Mark where platelets are.
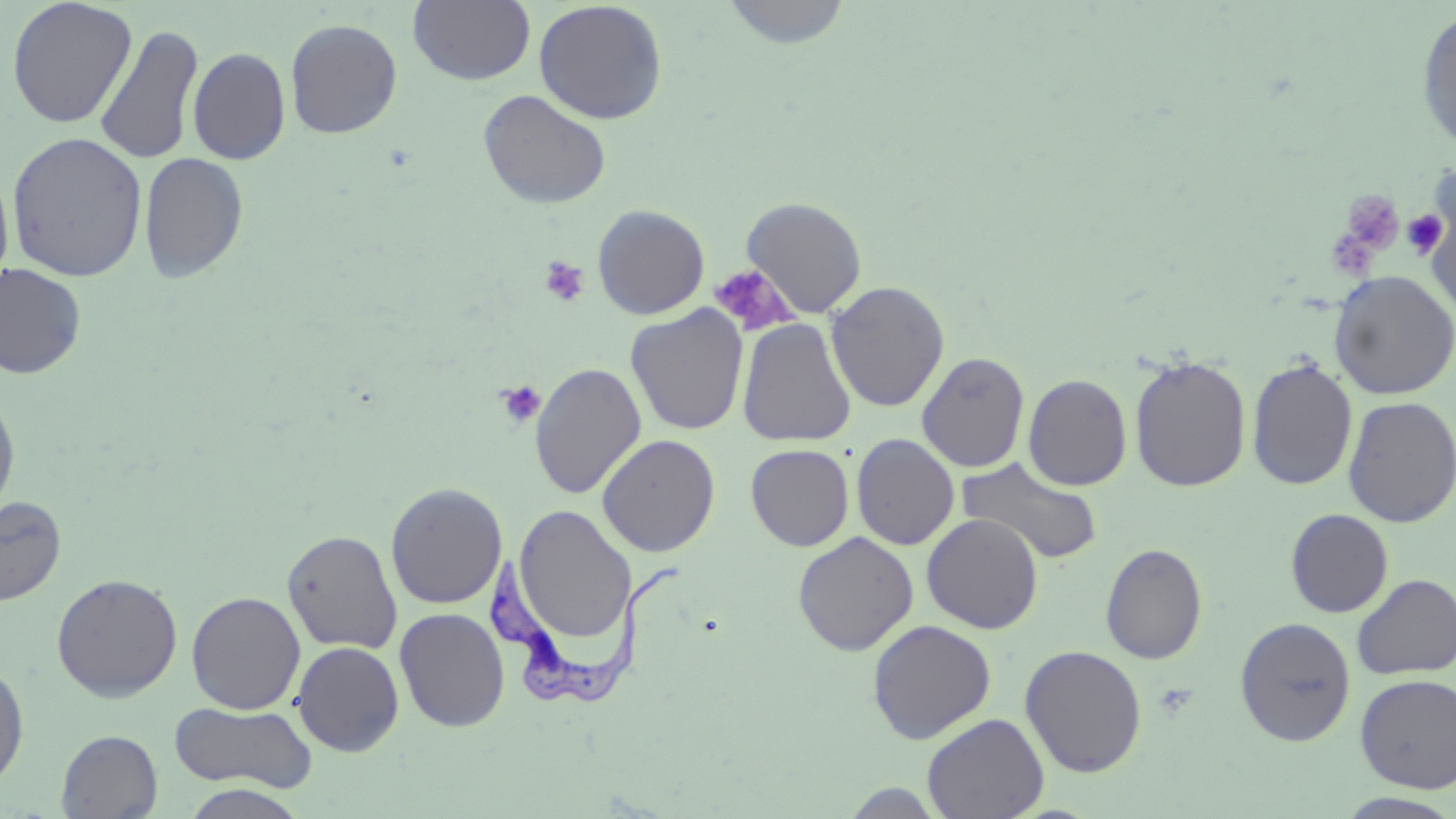
Approximate bounding boxes as (x1, y1, x2, y2) in pixels.
Platelets: (1338, 188, 1403, 256), (1402, 207, 1450, 261), (1327, 234, 1377, 281), (539, 256, 590, 307), (708, 263, 797, 336), (495, 380, 546, 429).

{
  "slide_level_diagnosis": "Trypanosoma brucei",
  "modality": "light microscopy",
  "magnification": "1000x",
  "preparation": "thin blood film",
  "image_size": "1456×819 pixels",
  "uninfected_red_blood_cell_locations": "approximate bounding boxes as (x1, y1, x2, y2) in pixels: (6, 0, 138, 128), (408, 0, 536, 85), (721, 0, 853, 49), (533, 1, 668, 125), (1415, 8, 1456, 156), (285, 18, 403, 138), (93, 24, 205, 165), (187, 47, 291, 165), (477, 89, 612, 209), (6, 131, 148, 282), (139, 151, 249, 284), (0, 161, 15, 295), (741, 196, 867, 318), (592, 204, 710, 320), (0, 263, 87, 379), (1329, 271, 1456, 399), (825, 280, 949, 412), (627, 305, 749, 436), (737, 318, 856, 447), (917, 352, 1030, 472), (1129, 354, 1252, 493), (1246, 357, 1358, 492), (529, 361, 647, 500), (1023, 373, 1132, 491), (0, 392, 20, 521), (1342, 395, 1456, 528), (851, 433, 959, 550), (597, 434, 720, 556), (745, 444, 854, 550), (956, 457, 1104, 566), (385, 482, 507, 610), (0, 495, 67, 606), (513, 505, 636, 647), (1285, 508, 1394, 618), (921, 514, 1044, 633), (282, 529, 403, 654), (793, 531, 919, 655), (1100, 542, 1208, 665), (51, 573, 183, 703), (1352, 573, 1456, 679), (185, 591, 307, 714), (394, 607, 510, 732), (1235, 616, 1356, 746), (867, 619, 996, 744), (292, 641, 405, 756), (1020, 645, 1147, 778), (0, 662, 30, 789), (1354, 673, 1456, 794), (169, 701, 318, 794), (922, 712, 1049, 819), (57, 730, 162, 818), (839, 782, 948, 818), (178, 784, 312, 819), (1334, 792, 1456, 819)",
  "trypanosoma_brucei_locations": "approximate bounding boxes as (x1, y1, x2, y2) in pixels: (488, 551, 683, 710)",
  "field_of_view": "single",
  "stain": "May-Grünwald-Giemsa"
}